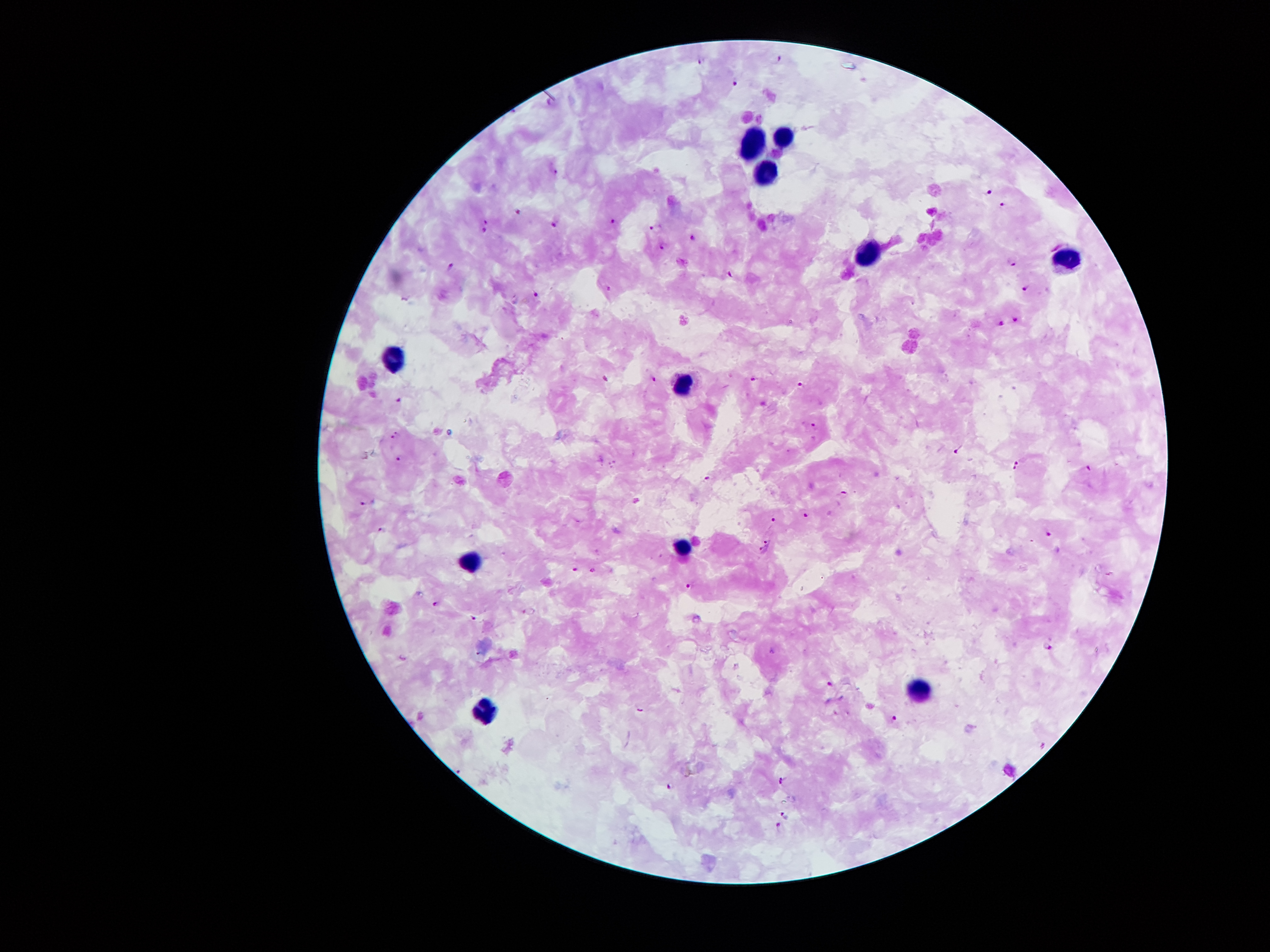

Approximate centers as {x, y} in pixels. Leukocyte locations: {786, 137}, {754, 142}, {767, 170}, {868, 253}, {1067, 260}, {395, 359}, {683, 386}, {688, 547}, {474, 559}, {921, 686}, {483, 708}. Malaria parasite locations: {780, 57}, {700, 60}, {734, 83}, {556, 170}, {990, 192}, {1002, 204}, {518, 211}, {485, 221}, {614, 222}, {555, 225}, {655, 228}, {484, 230}, {695, 239}, {661, 245}, {1014, 260}, {451, 266}, {730, 274}, {1026, 287}, {609, 288}, {536, 295}, {1016, 319}, {1001, 323}, {655, 378}, {606, 379}, {754, 379}, {801, 385}, {399, 401}, {814, 427}, {397, 435}, {957, 451}, {398, 458}, {1016, 461}, {1089, 467}, {1014, 468}, {706, 477}, {843, 494}, {367, 503}, {806, 515}, {772, 520}, {383, 529}, {1049, 535}, {768, 541}, {762, 550}, {574, 569}, {593, 569}, {689, 586}, {439, 603}, {474, 616}, {1049, 647}, {831, 685}, {639, 711}, {896, 718}, {1044, 746}, {460, 771}, {783, 780}, {670, 787}, {787, 813}, {779, 826}. Image is 1270×952 pixels. Patient malaria status: infected with Plasmodium falciparum. One field from this slide. Thick blood smear. 100x magnification. Giemsa-stained preparation. Photographed through the microscope eyepiece with a smartphone camera.